Report the malaria status of this cell.
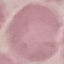

Uninfected.

Photographed with a smartphone camera at the microscope eyepiece. Automatically extracted cell patch, resized to 64 × 64 pixels. Thin blood smear. Giemsa-stained preparation.